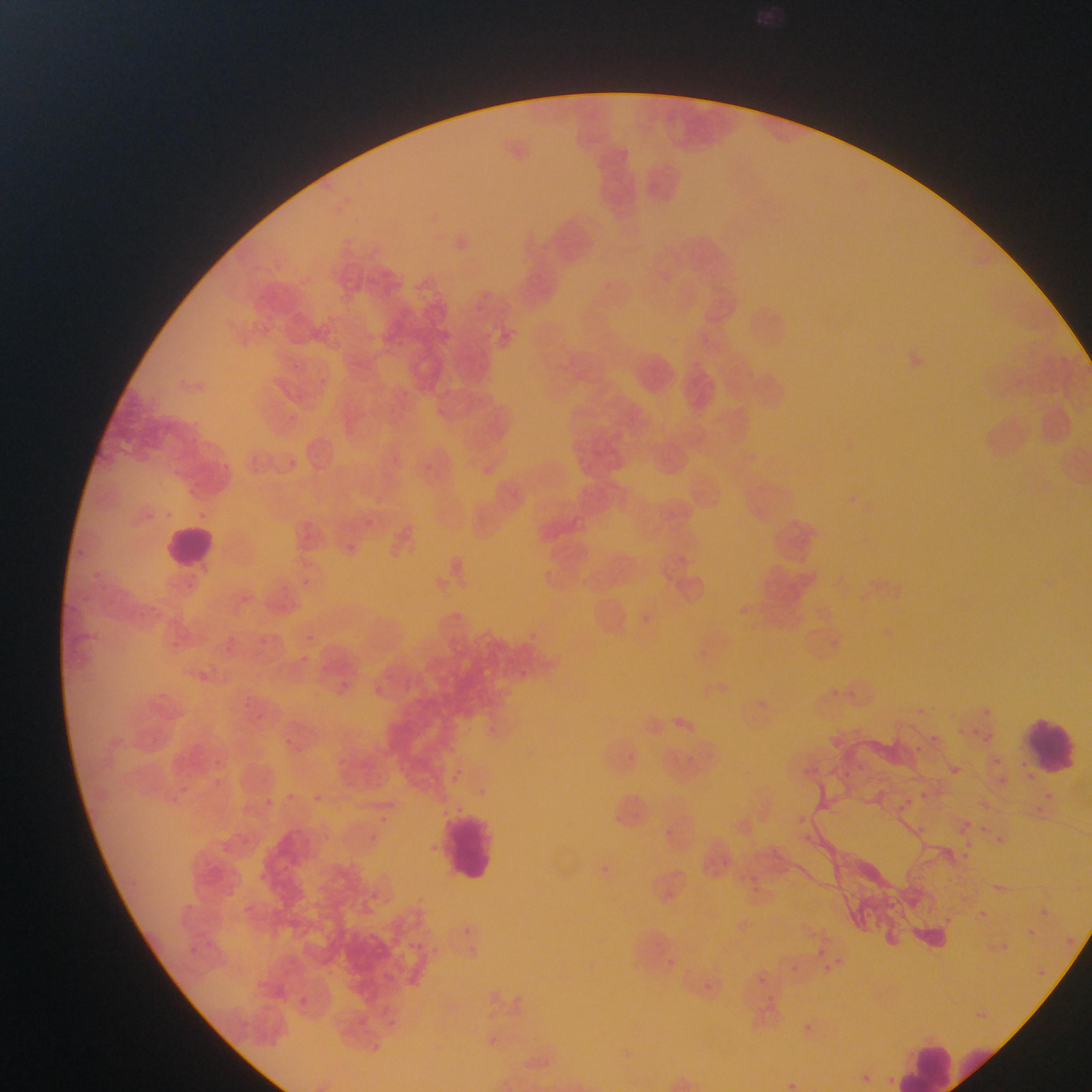

Approximate bounding boxes as (left, top, right, bottom) in pixels. Malaria parasite locations: (289, 459, 297, 467), (364, 519, 373, 528), (225, 631, 243, 649), (298, 631, 325, 643), (166, 636, 181, 653), (298, 655, 313, 668), (200, 668, 217, 685), (824, 679, 847, 710), (339, 680, 353, 693), (378, 682, 388, 692), (982, 708, 992, 718), (927, 723, 941, 752), (966, 723, 993, 745), (277, 729, 302, 755), (912, 738, 930, 768), (854, 754, 875, 780), (995, 754, 1002, 762), (935, 758, 961, 781), (808, 759, 822, 777), (452, 767, 462, 782), (214, 773, 236, 799), (996, 774, 1014, 792), (180, 782, 200, 804), (920, 782, 941, 806), (310, 790, 323, 804), (285, 792, 295, 802), (265, 798, 275, 807), (1035, 801, 1053, 817), (899, 802, 915, 820), (798, 815, 809, 826), (373, 816, 394, 834), (964, 821, 973, 830), (910, 823, 928, 843), (798, 834, 825, 851), (962, 837, 976, 848), (958, 852, 974, 870), (598, 862, 616, 875), (747, 865, 770, 894), (975, 904, 994, 925), (1040, 905, 1048, 912), (1025, 918, 1039, 939), (458, 923, 474, 935), (994, 938, 1010, 951), (415, 939, 442, 972), (817, 942, 828, 956), (834, 950, 845, 966), (783, 959, 809, 977), (812, 962, 837, 979), (754, 971, 763, 979), (292, 993, 315, 1015), (772, 1001, 783, 1009), (351, 1007, 375, 1025), (793, 1017, 815, 1033), (368, 1041, 380, 1053), (883, 1067, 894, 1080), (854, 1072, 874, 1090). Leukocyte locations: (162, 523, 220, 576), (1025, 718, 1076, 770), (443, 813, 495, 879), (898, 1040, 987, 1092). Image is 1092×1092 pixels. Mobile-phone photograph taken through the microscope. Collected in Ghana. Single field of view. Thin blood film.